Classify this cell by malaria status.
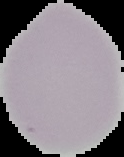

Uninfected.

Summary:
  - Image type: segmented cell region on a black background
  - Preparation: thin blood smear
  - Image size: 124×157 pixels